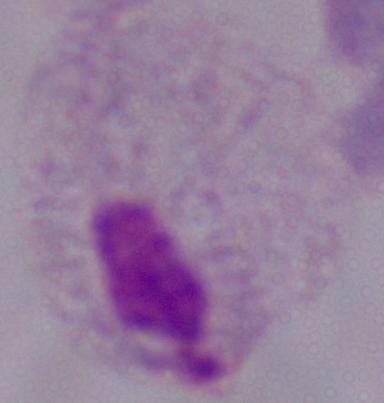 A trichomonad is seen. Micrograph. 1000x magnification.